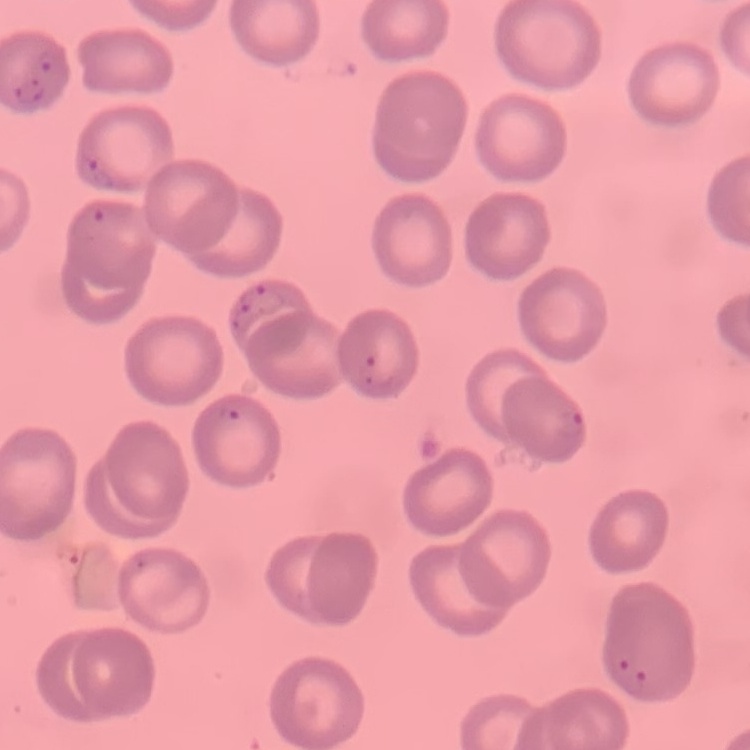 The red blood cells show no rouleaux formation. One tile cut from a larger photomicrograph. Thin peripheral smear. Field's or Giemsa stain.